Identify the blood parasite species.
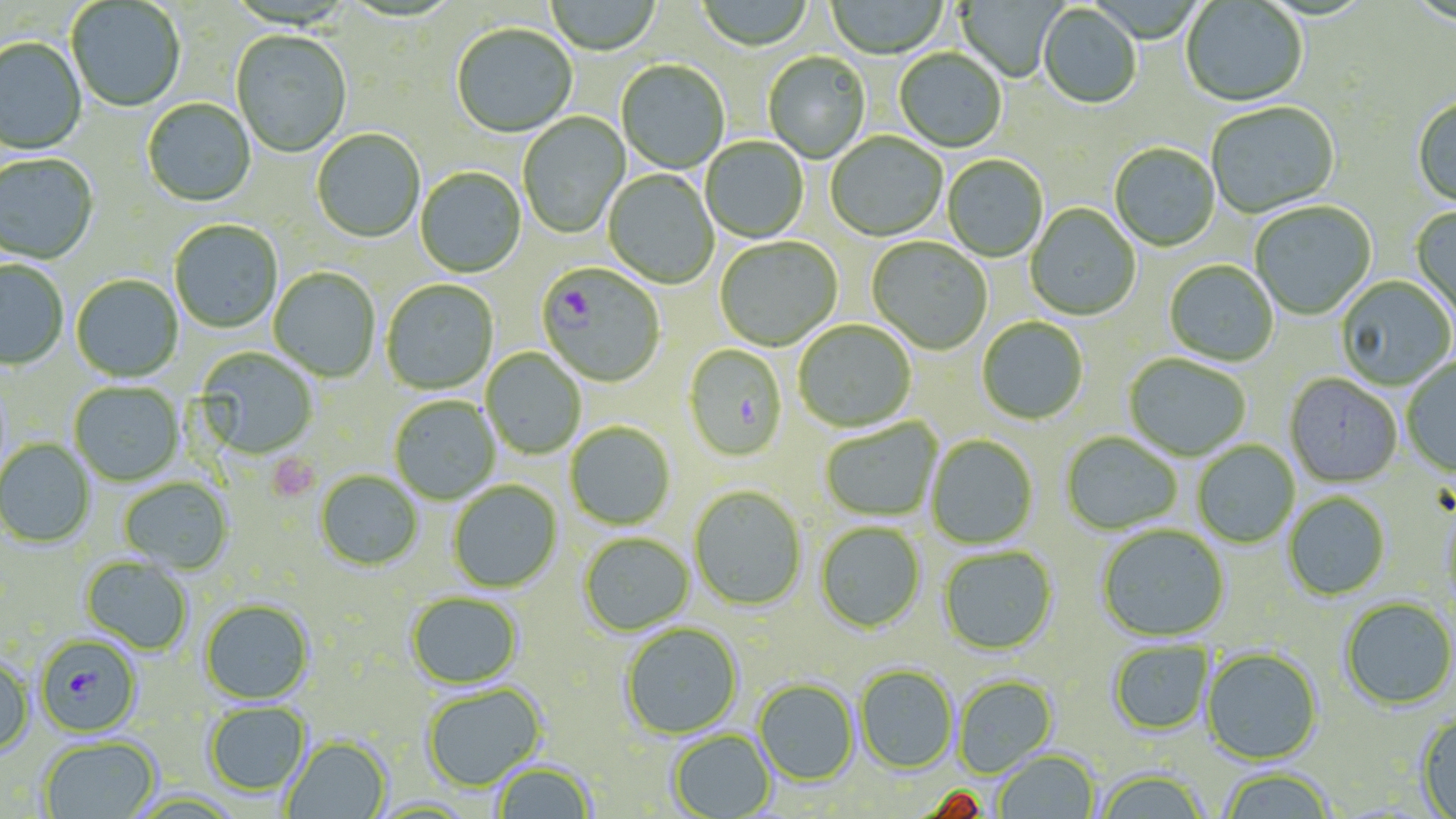

Plasmodium falciparum.

Approximate bounding boxes as named x1/y1/x2/y2 corners in pixels. Plasmodium falciparum-infected red blood cell locations: (x1=537, y1=262, x2=666, y2=388), (x1=34, y1=634, x2=142, y2=737). Platelet locations: (x1=267, y1=453, x2=321, y2=503). Uninfected red blood cell locations: (x1=545, y1=0, x2=661, y2=56), (x1=696, y1=0, x2=814, y2=52), (x1=826, y1=0, x2=948, y2=60), (x1=955, y1=0, x2=1063, y2=82), (x1=67, y1=1, x2=185, y2=113), (x1=1181, y1=1, x2=1308, y2=109), (x1=1038, y1=6, x2=1141, y2=110), (x1=450, y1=25, x2=579, y2=138), (x1=231, y1=31, x2=352, y2=159), (x1=0, y1=38, x2=87, y2=156), (x1=894, y1=49, x2=1007, y2=153), (x1=763, y1=53, x2=870, y2=163), (x1=616, y1=61, x2=729, y2=174), (x1=142, y1=99, x2=256, y2=208), (x1=1411, y1=99, x2=1456, y2=210), (x1=1206, y1=102, x2=1340, y2=220), (x1=518, y1=112, x2=630, y2=239), (x1=311, y1=130, x2=425, y2=244), (x1=825, y1=133, x2=947, y2=242), (x1=701, y1=137, x2=809, y2=243), (x1=1109, y1=144, x2=1220, y2=252), (x1=0, y1=155, x2=99, y2=265), (x1=942, y1=156, x2=1048, y2=262), (x1=415, y1=167, x2=526, y2=278), (x1=603, y1=170, x2=718, y2=289), (x1=1249, y1=202, x2=1376, y2=320), (x1=1026, y1=204, x2=1140, y2=321), (x1=1411, y1=206, x2=1456, y2=324), (x1=169, y1=220, x2=283, y2=334), (x1=715, y1=237, x2=841, y2=351), (x1=867, y1=238, x2=992, y2=355), (x1=0, y1=260, x2=68, y2=369), (x1=1164, y1=260, x2=1279, y2=367), (x1=269, y1=267, x2=381, y2=382), (x1=71, y1=275, x2=183, y2=383), (x1=1336, y1=276, x2=1455, y2=390), (x1=381, y1=279, x2=499, y2=395), (x1=977, y1=317, x2=1088, y2=424), (x1=793, y1=319, x2=917, y2=432), (x1=683, y1=344, x2=788, y2=461), (x1=196, y1=347, x2=318, y2=459), (x1=482, y1=349, x2=586, y2=459), (x1=1124, y1=354, x2=1251, y2=461), (x1=1402, y1=358, x2=1456, y2=477), (x1=1284, y1=374, x2=1402, y2=487), (x1=70, y1=383, x2=184, y2=487), (x1=389, y1=396, x2=500, y2=505), (x1=820, y1=419, x2=943, y2=522), (x1=565, y1=422, x2=675, y2=529), (x1=1060, y1=431, x2=1183, y2=535), (x1=926, y1=434, x2=1038, y2=549), (x1=0, y1=439, x2=95, y2=548), (x1=1192, y1=441, x2=1299, y2=548), (x1=315, y1=470, x2=423, y2=570), (x1=119, y1=477, x2=233, y2=572), (x1=448, y1=481, x2=562, y2=593), (x1=689, y1=486, x2=807, y2=611), (x1=1283, y1=492, x2=1390, y2=600), (x1=1439, y1=502, x2=1456, y2=612), (x1=816, y1=521, x2=926, y2=633), (x1=1096, y1=524, x2=1230, y2=642), (x1=579, y1=532, x2=694, y2=636), (x1=938, y1=545, x2=1057, y2=655), (x1=81, y1=557, x2=193, y2=654), (x1=406, y1=592, x2=522, y2=689), (x1=1339, y1=597, x2=1456, y2=710), (x1=200, y1=599, x2=314, y2=704), (x1=620, y1=622, x2=743, y2=739), (x1=1108, y1=639, x2=1214, y2=736), (x1=1201, y1=646, x2=1323, y2=764), (x1=0, y1=656, x2=33, y2=757), (x1=855, y1=665, x2=957, y2=773), (x1=953, y1=675, x2=1058, y2=777), (x1=754, y1=679, x2=859, y2=786), (x1=421, y1=683, x2=545, y2=792), (x1=204, y1=701, x2=310, y2=797), (x1=1415, y1=714, x2=1456, y2=819), (x1=668, y1=729, x2=775, y2=819), (x1=39, y1=736, x2=160, y2=819), (x1=281, y1=736, x2=390, y2=819), (x1=994, y1=749, x2=1100, y2=818), (x1=491, y1=761, x2=595, y2=819), (x1=1217, y1=767, x2=1336, y2=819), (x1=1094, y1=769, x2=1211, y2=819). 1000x magnification. One field of a larger specimen. May-Grünwald-Giemsa stain. Light microscopy. Image is 1456×819 pixels. Thin blood smear.